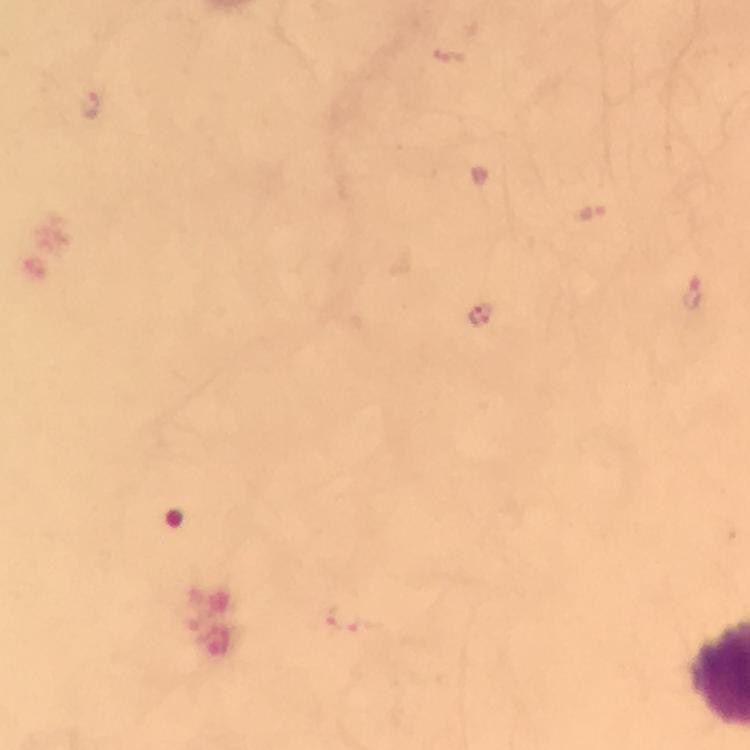

{
  "preparation": "thick smear",
  "immersion_oil": "applied",
  "malaria_parasite_locations": "approximate centers as [x, y] in pixels: [90, 107], [589, 212], [693, 292], [481, 316], [342, 618]",
  "context": "from a malaria diagnostic workup",
  "image_size": "750×750 pixels",
  "stain": "Giemsa",
  "cropped_from": "a single field of view",
  "magnification": "100x",
  "capture": "smartphone photograph through a microscope"
}